Comment on the morphology of the red blood cells.
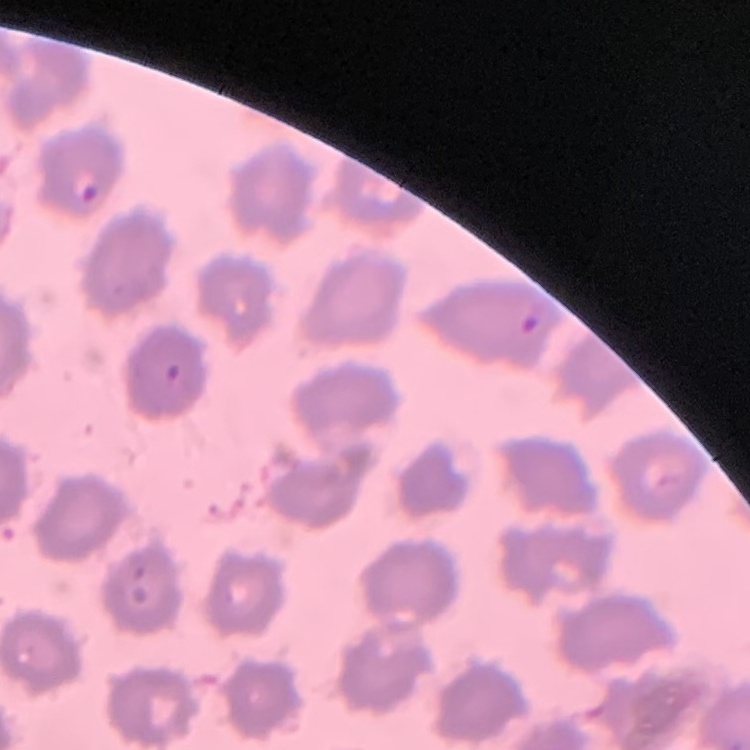

No rouleaux formation.

Summary:
  - Preparation: thin blood film
  - Stain: Field's or Giemsa
  - Image type: square crop of a larger photomicrograph